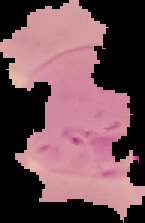

Summary:
  - Result: Plasmodium parasites identified
  - Preparation: thin blood smear
  - Image size: 145×223 pixels
  - Image type: segmented cell region on a black background